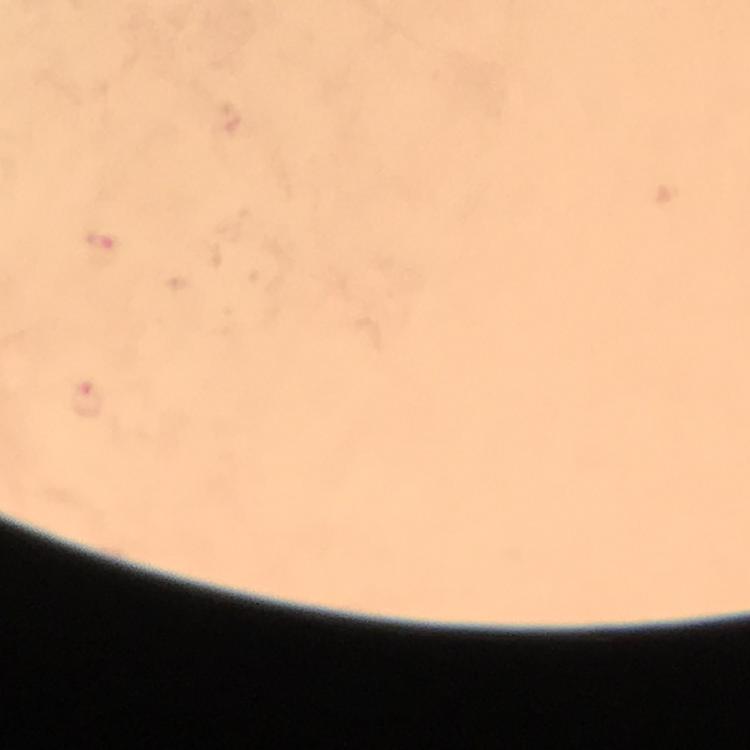 Approximate centers as {x, y} in pixels. Plasmodium parasite locations: {101, 246}, {88, 401}. Thick blood film. Smartphone photograph taken through a microscope. Cropped region of a single field of view. Image is 750×750 pixels. Giemsa stain. From a malaria diagnostic workup. 100x magnification. Immersion oil applied.